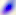
magnification = 400x
modality = micrograph
identification = Toxoplasma gondii